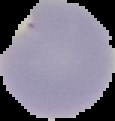

From a thin blood smear. The area outside the segmented cell region is set to black. Image is 115×121 pixels. Malaria status: parasitized.